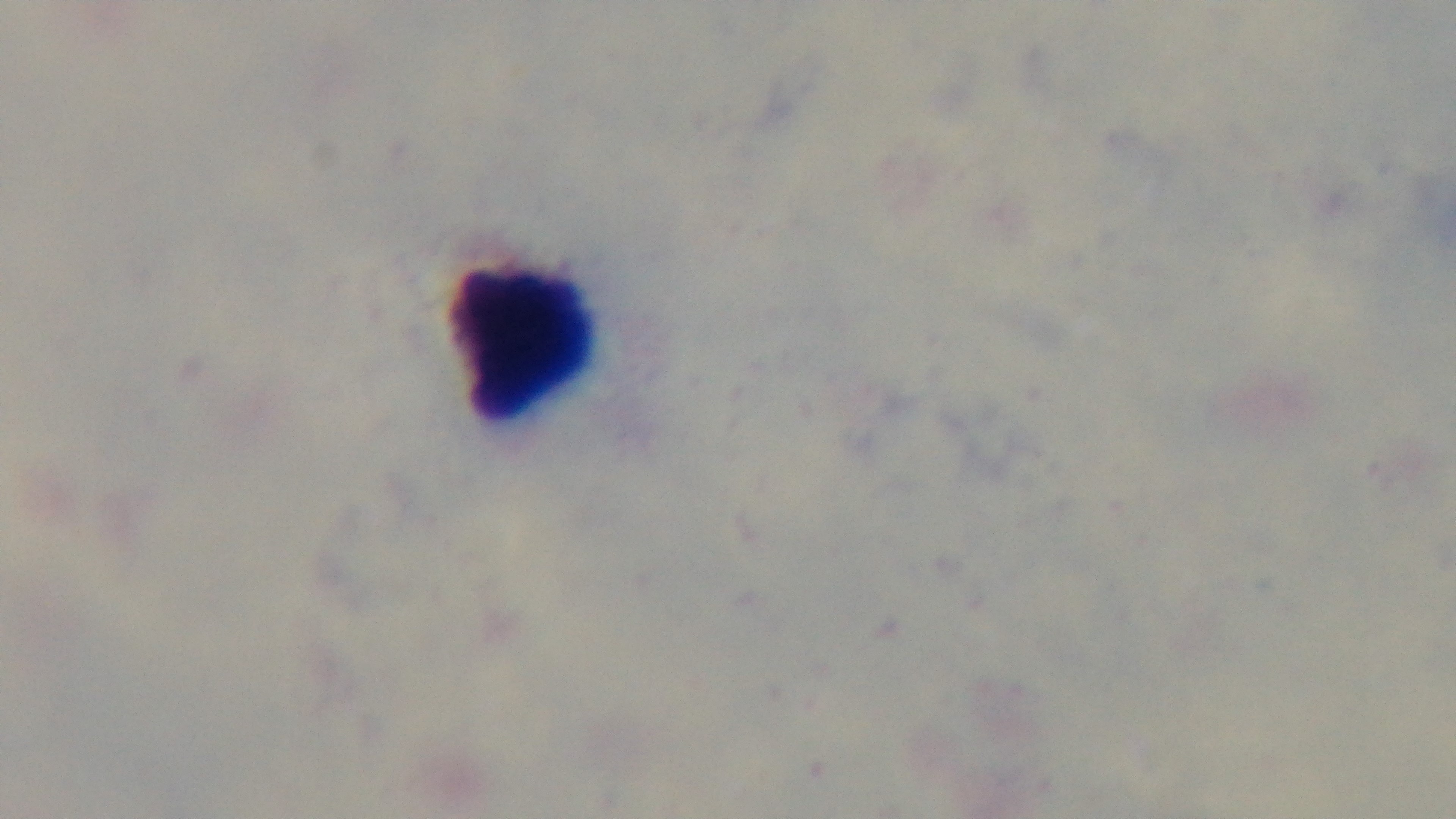
{
  "modality": "light microscopy",
  "field_of_view": "single",
  "preparation": "thick",
  "capture": "mounted 4K digital camera",
  "stain": "Giemsa",
  "malaria_status": "uninfected",
  "objective": "100x oil immersion"
}